Identify the parasite.
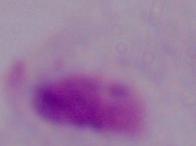

This is a trichomonad.

magnification = 1000x
modality = micrograph